Assess for malaria.
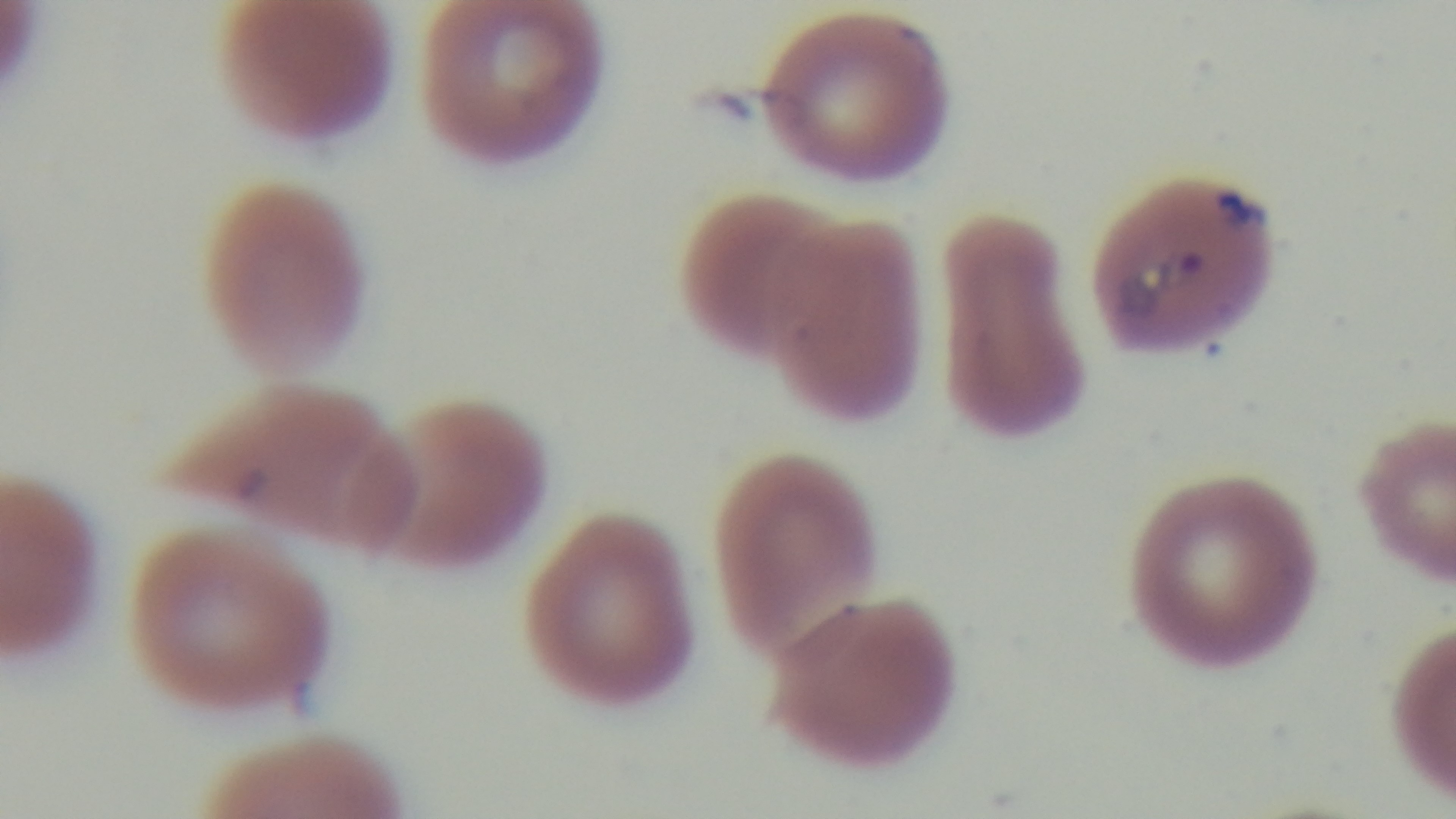
Infected.

Summary:
  - Objective: 100x oil immersion
  - Field of view: one from the slide
  - Stain: Giemsa
  - Preparation: thin smear
  - Modality: light microscopy
  - Capture: mounted 4K digital camera